Classify this cell by malaria status.
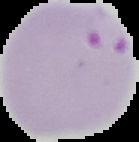
Parasitized.

Summary:
  - Preparation: thin blood smear
  - Image type: segmented cell region on a black background
  - Image size: 139×142 pixels